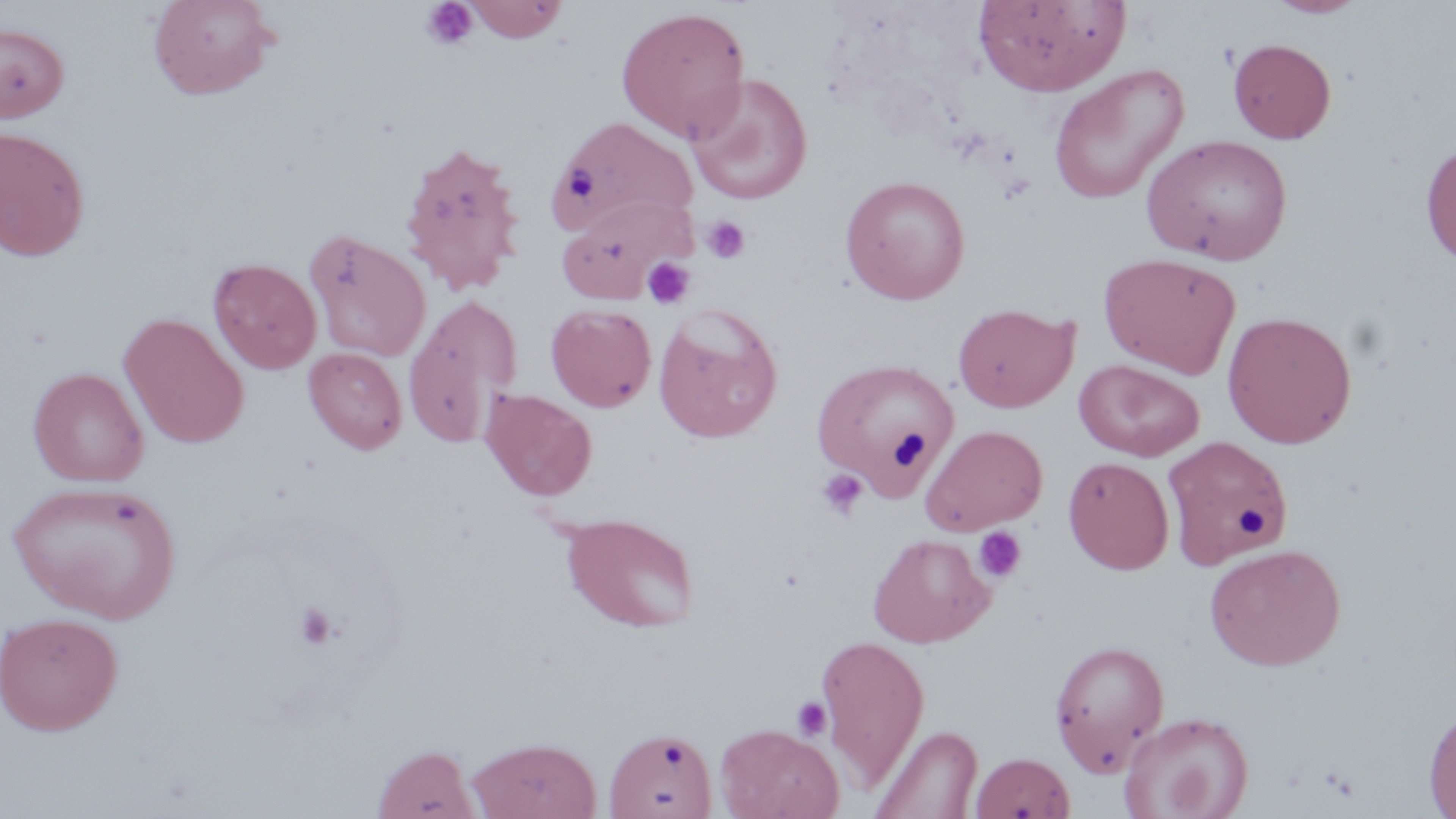

Approximate bounding boxes as (x1, y1, x2, y2) in pixels. Uninfected red blood cell locations: (147, 0, 278, 100), (465, 0, 568, 42), (974, 0, 1130, 96), (1265, 0, 1368, 18), (615, 6, 751, 142), (0, 23, 70, 123), (1228, 38, 1336, 144), (1048, 64, 1189, 204), (685, 73, 813, 205), (545, 116, 699, 241), (0, 126, 91, 261), (1141, 133, 1293, 265), (398, 138, 526, 295), (1421, 139, 1456, 268), (841, 176, 970, 304), (556, 198, 690, 303), (305, 229, 431, 362), (1099, 252, 1241, 378), (208, 258, 322, 374), (404, 295, 522, 446), (546, 303, 656, 412), (953, 303, 1077, 413), (653, 305, 783, 443), (1222, 310, 1358, 448), (119, 312, 249, 448), (303, 347, 407, 454), (812, 358, 959, 493), (1075, 359, 1204, 461), (28, 367, 148, 487), (481, 389, 597, 501), (921, 424, 1048, 535), (1162, 435, 1292, 570), (1063, 456, 1175, 574), (8, 479, 181, 624), (560, 512, 699, 633), (868, 533, 994, 648), (1204, 543, 1346, 670), (0, 612, 123, 736), (815, 633, 930, 789), (1049, 638, 1170, 774), (1424, 702, 1456, 818), (1119, 711, 1254, 819), (715, 723, 843, 819), (872, 724, 983, 819), (604, 727, 718, 818), (468, 737, 602, 818), (371, 744, 480, 819), (971, 752, 1075, 818). Platelet locations: (420, 1, 478, 51), (702, 216, 752, 264), (643, 257, 694, 308), (817, 468, 867, 520), (973, 526, 1027, 584), (294, 603, 338, 649), (792, 697, 833, 740). Slide-level diagnosis: no evidence of blood parasites. Light microscopy. Captured at 1000x magnification. Image is 1456×819 pixels. May-Grünwald-Giemsa stain. Thin blood smear. Single field of view.